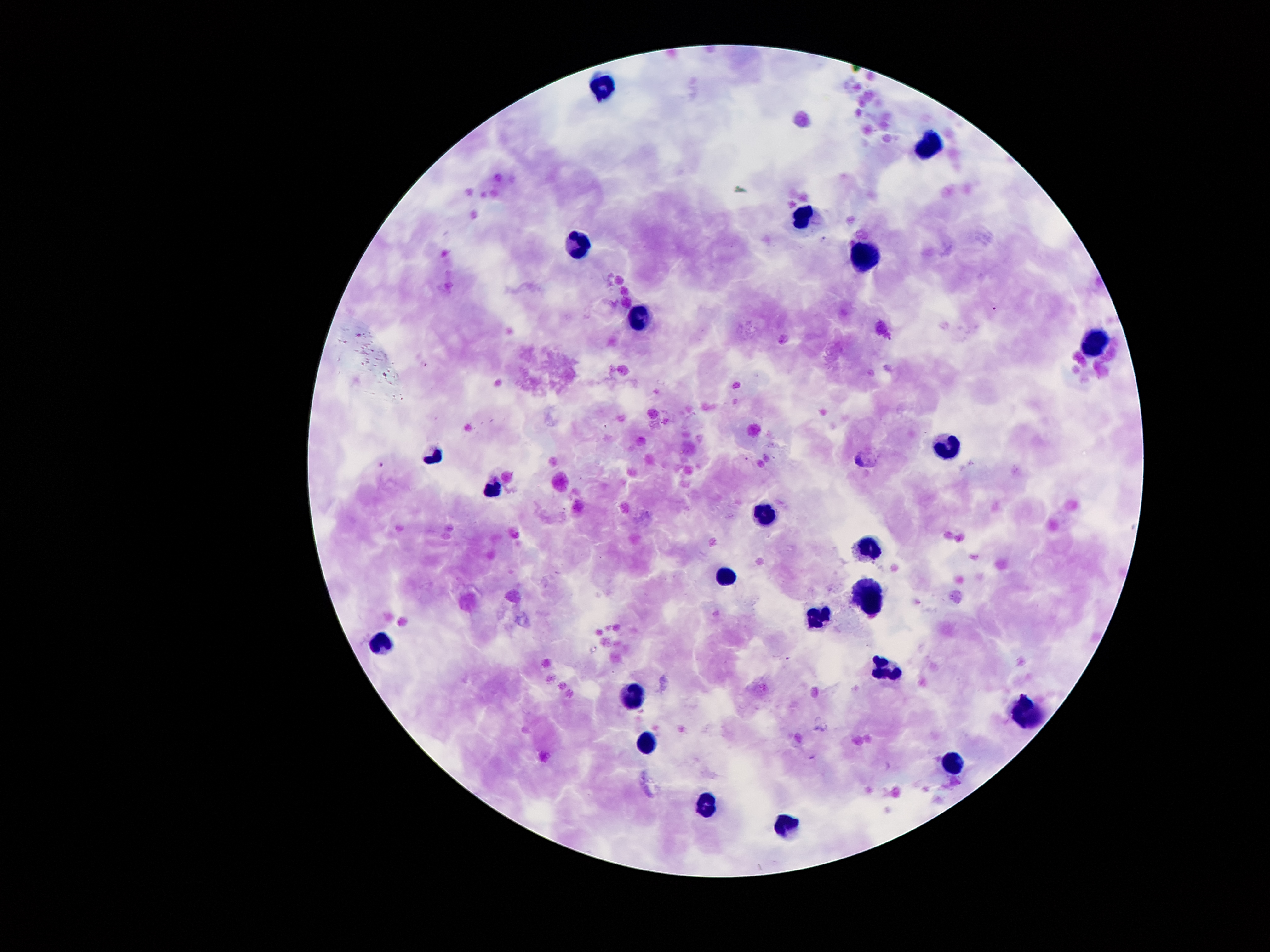

Approximate centers as {x, y} in pixels. Malaria parasite locations: {859, 459}, {381, 466}. Leukocyte locations: {602, 84}, {931, 146}, {802, 217}, {576, 248}, {865, 254}, {636, 322}, {1094, 340}, {948, 445}, {433, 453}, {496, 488}, {765, 509}, {866, 547}, {729, 576}, {866, 592}, {816, 615}, {384, 641}, {880, 666}, {631, 695}, {1022, 711}, {646, 745}, {949, 763}, {705, 803}, {782, 827}. Thick peripheral-blood smear. Patient malaria status: infected with Plasmodium falciparum. Giemsa-stained preparation. One field from this slide. Smartphone photograph taken through the microscope eyepiece. 100x magnification. Image is 1270×952 pixels.